Evaluate for malaria.
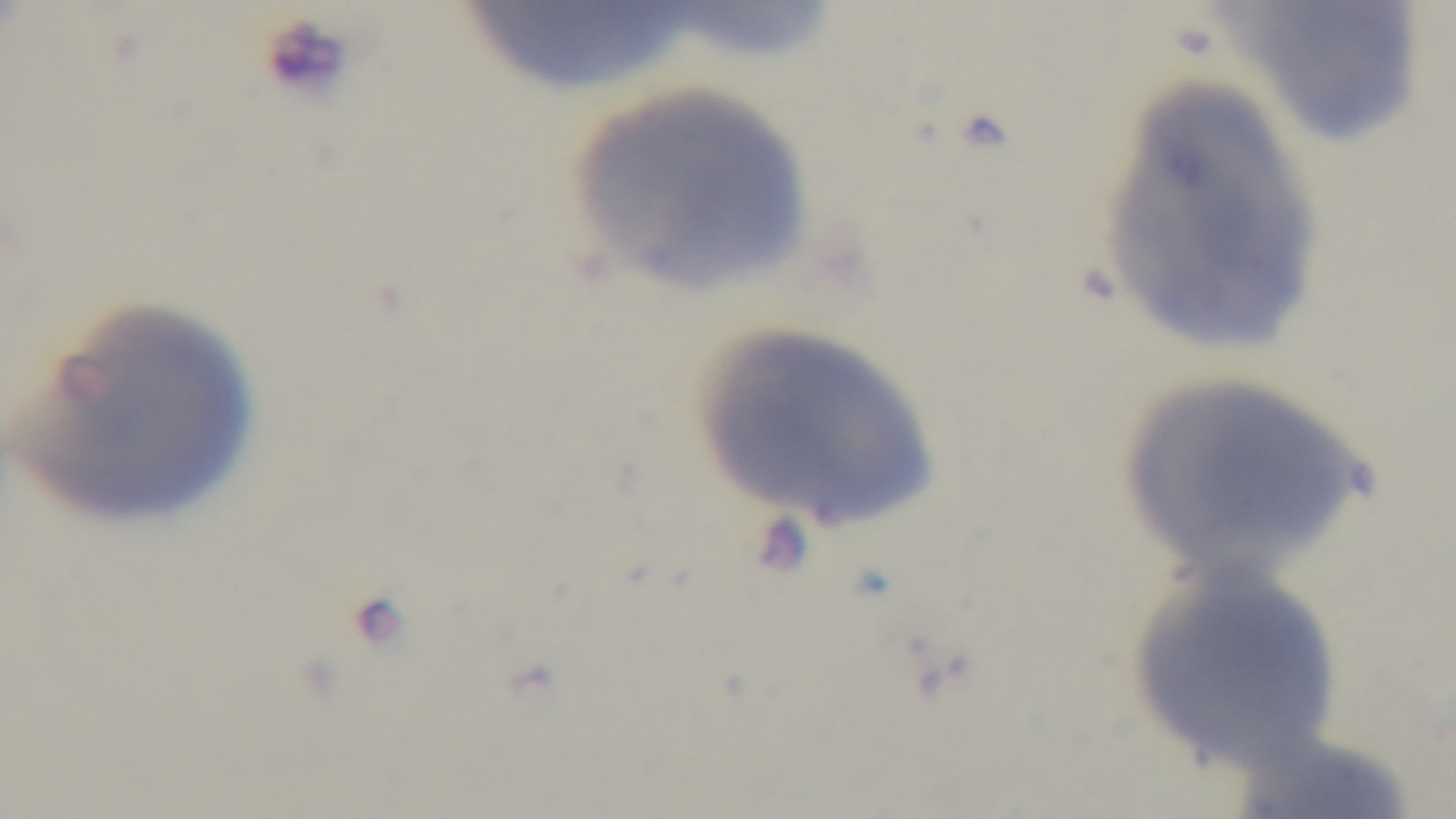
Negative.

Summary:
  - Capture: mounted 4K digital camera
  - Modality: light microscopy
  - Preparation: thin blood film
  - Field of view: single
  - Objective: 100x oil immersion
  - Stain: Giemsa